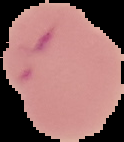 Cell region segmented out of the field of view; the surrounding area is masked to black. From a thin blood film. Image is 124×142 pixels. Result: malaria parasites detected.